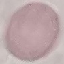

Summary:
  - Malaria status: uninfected
  - Preparation: thin blood smear
  - Image type: cell patch, automatically extracted from a larger field of view and resized to 64 × 64 pixels
  - Stain: Giemsa
  - Capture: smartphone through the microscope eyepiece